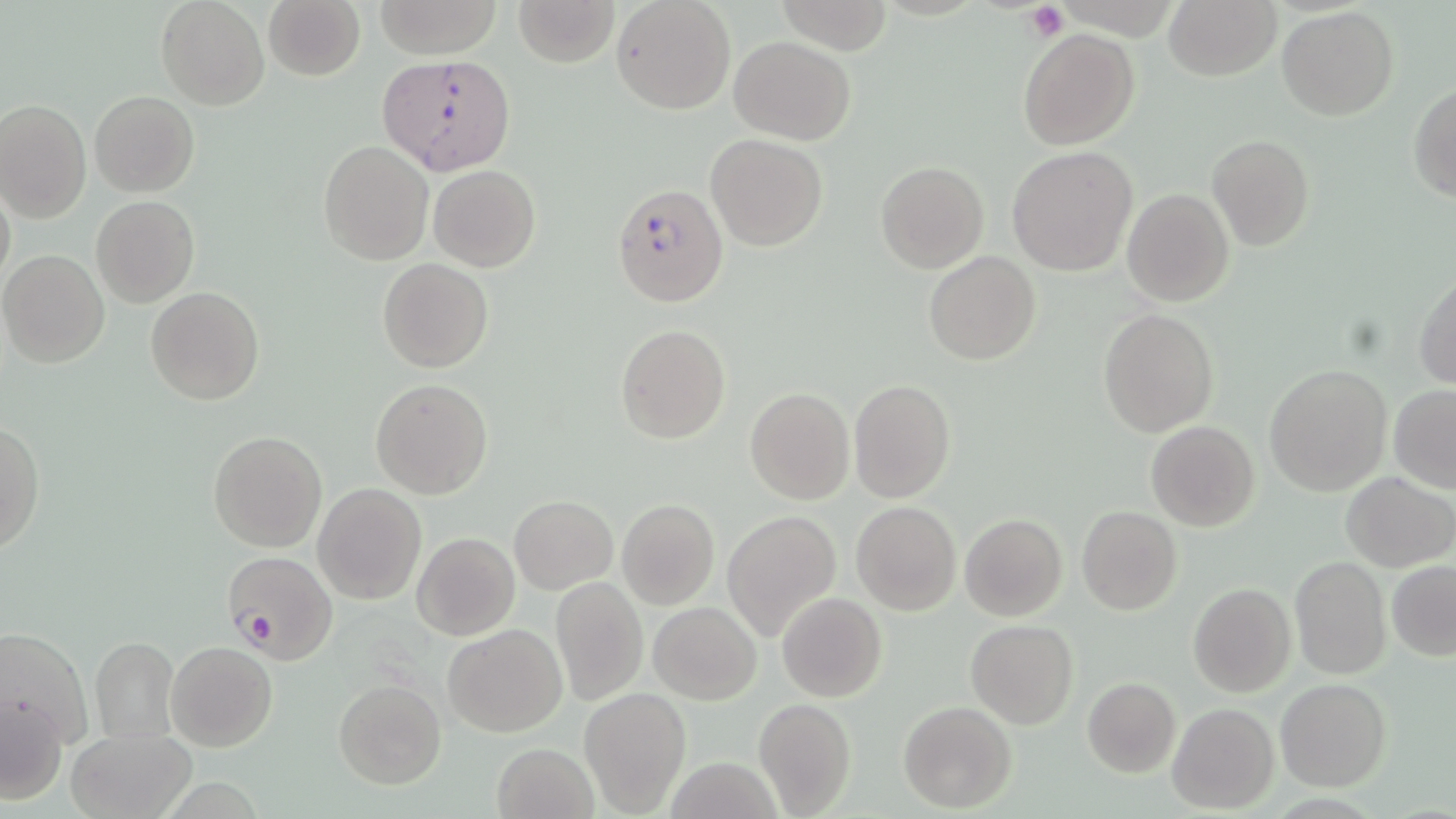
Summary:
  - Coordinate format: approximate bounding boxes as (x1,y1)-(x2,y2) corner pairs in pixels
  - Plasmodium falciparum-infected red blood cell locations: (379,53)-(517,179), (611,180)-(727,307), (219,550)-(337,664)
  - Uninfected red blood cell locations: (156,0)-(269,110), (262,0)-(365,81), (372,0)-(503,57), (514,0)-(620,68), (612,0)-(736,114), (1164,0)-(1281,81), (776,1)-(892,54), (1278,5)-(1398,119), (1018,28)-(1140,150), (728,36)-(856,146), (1408,83)-(1456,201), (88,91)-(199,197), (0,99)-(91,221), (706,134)-(828,250), (1207,135)-(1315,253), (319,141)-(431,264), (1006,146)-(1138,276), (876,162)-(989,274), (429,165)-(540,272), (0,180)-(15,296), (1121,188)-(1233,308), (91,195)-(199,308), (0,250)-(112,368), (924,251)-(1040,366), (377,258)-(492,373), (1412,272)-(1456,388), (145,286)-(265,405), (1098,309)-(1218,438), (616,324)-(731,444), (1264,364)-(1392,495), (370,378)-(493,499), (849,378)-(956,503), (1388,384)-(1456,492), (744,387)-(856,504), (0,421)-(45,557), (1145,421)-(1260,532), (207,430)-(327,552), (1340,472)-(1454,572), (314,484)-(426,603), (509,495)-(618,594), (615,499)-(719,611), (850,501)-(961,616), (1077,505)-(1183,615), (722,510)-(841,640), (959,512)-(1068,622), (413,532)-(519,640), (1289,554)-(1391,680), (1387,561)-(1456,661), (551,578)-(646,706), (1189,583)-(1296,698), (777,592)-(887,703), (648,600)-(762,705), (966,620)-(1077,730), (443,623)-(567,736), (1,627)-(92,754), (90,636)-(179,742), (166,642)-(278,752), (1082,676)-(1181,776), (1276,679)-(1391,792), (333,680)-(446,788), (579,689)-(689,815), (2,693)-(68,807), (753,698)-(857,817), (898,701)-(1016,812), (1168,703)-(1279,814), (66,727)-(195,818), (491,742)-(600,819)
  - Platelet locations: (1026,3)-(1069,42)
  - Slide-level diagnosis: Plasmodium falciparum
  - Image size: 1456×819 pixels
  - Field of view: one of a larger specimen
  - Stain: May-Grünwald-Giemsa
  - Preparation: thin blood smear
  - Modality: light microscopy
  - Magnification: 1000x